Assess the morphology of the erythrocytes.
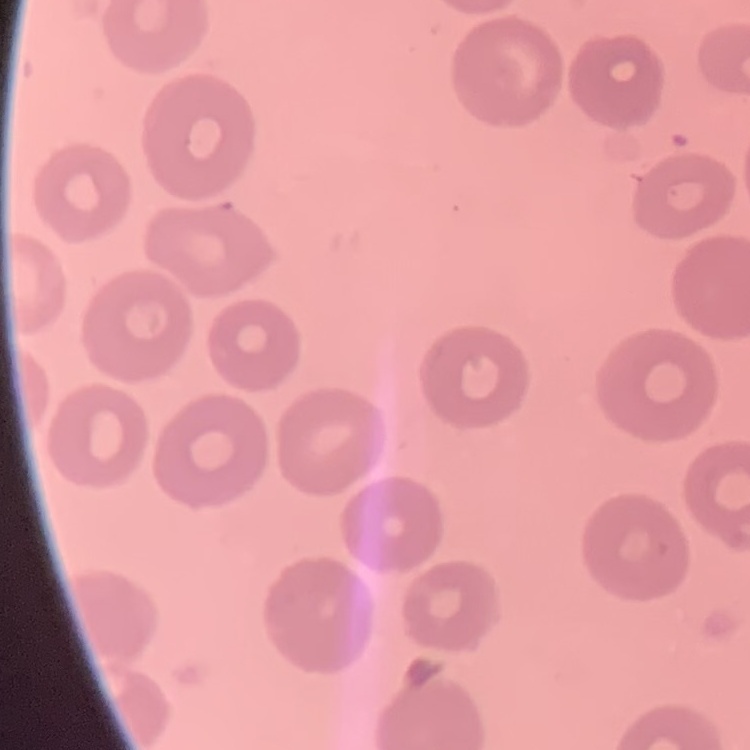
No rouleaux formation.

{
  "stain": "Field's or Giemsa",
  "image_type": "square crop of a larger photomicrograph",
  "preparation": "thin blood film"
}